Classify this cell by malaria status.
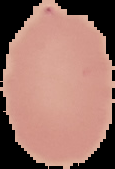
It is uninfected.

From a thin blood smear. Segmented cell region on a black background. Image is 115×169 pixels.